State the blood parasite species.
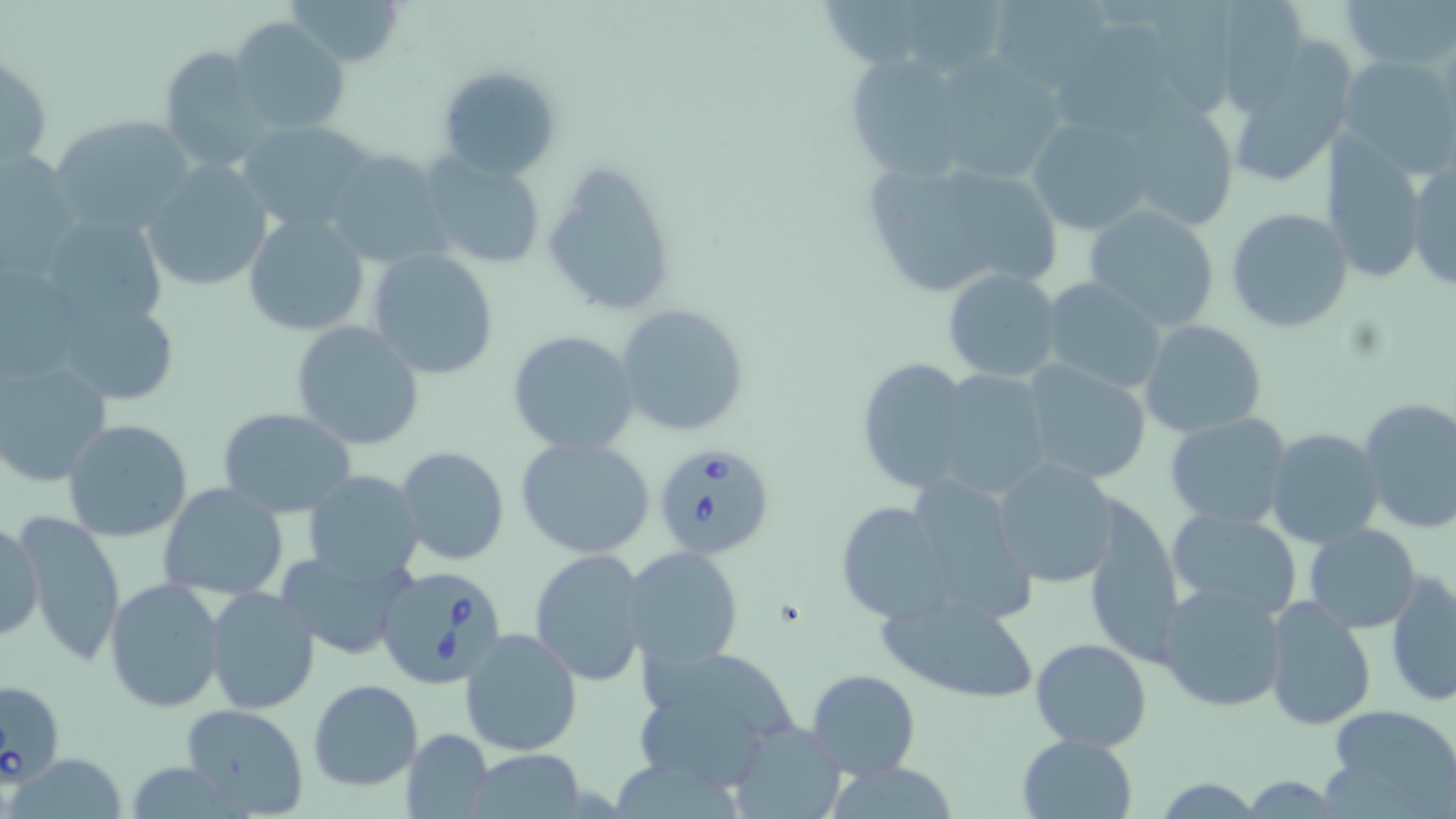
Babesia divergens.

preparation = thin blood film
image size = 1456×819 pixels
modality = light microscopy
magnification = 1000x
stain = May-Grünwald-Giemsa
Babesia divergens-infected red blood cell locations = approximate bounding boxes as [x1, y1, x2, y2] in pixels: [650, 440, 778, 561], [372, 562, 511, 692]
uninfected red blood cell locations = approximate bounding boxes as [x1, y1, x2, y2] in pixels: [286, 0, 408, 68], [902, 0, 1004, 81], [1225, 0, 1312, 117], [1342, 0, 1453, 74], [1150, 1, 1243, 114], [826, 2, 931, 69], [996, 2, 1112, 85], [228, 18, 351, 135], [1059, 19, 1176, 134], [1224, 44, 1357, 192], [157, 47, 277, 175], [1, 51, 52, 175], [842, 53, 981, 182], [1336, 53, 1456, 178], [949, 56, 1066, 182], [437, 65, 560, 179], [1108, 95, 1243, 235], [1024, 110, 1163, 238], [49, 113, 196, 231], [240, 119, 379, 234], [1317, 139, 1428, 282], [321, 148, 451, 270], [1, 149, 82, 270], [419, 154, 546, 268], [1407, 155, 1455, 293], [541, 158, 676, 317], [142, 160, 274, 292], [958, 167, 1063, 290], [870, 171, 986, 293], [1083, 202, 1221, 331], [1226, 207, 1354, 333], [34, 211, 170, 335], [242, 211, 371, 338], [366, 248, 500, 380], [943, 267, 1065, 383], [1038, 278, 1171, 393], [40, 288, 186, 411], [615, 302, 749, 437], [1139, 320, 1267, 438], [290, 321, 425, 450], [505, 330, 639, 456], [855, 355, 978, 492], [0, 357, 112, 487], [1018, 360, 1153, 486], [915, 367, 1060, 500], [1356, 396, 1456, 535], [216, 407, 357, 519], [1163, 411, 1293, 531], [62, 417, 194, 541], [193, 424, 333, 570], [1264, 428, 1385, 548], [514, 435, 657, 559], [395, 446, 509, 566], [989, 458, 1121, 588], [304, 471, 426, 588], [891, 471, 1040, 631], [157, 483, 290, 599], [1084, 496, 1186, 665], [831, 502, 949, 624], [1165, 507, 1305, 620], [13, 511, 128, 667], [1, 516, 42, 644], [1304, 524, 1422, 632], [529, 546, 653, 686], [621, 546, 745, 671], [278, 548, 416, 661], [1386, 571, 1455, 707], [104, 578, 227, 712], [1156, 581, 1290, 713], [204, 586, 320, 715], [876, 589, 1041, 704], [1263, 596, 1376, 732], [460, 628, 583, 756], [1028, 638, 1152, 752], [640, 649, 807, 740], [806, 668, 921, 779], [1, 678, 66, 785], [306, 679, 424, 791], [630, 700, 769, 783], [178, 703, 309, 818], [1324, 704, 1456, 813], [729, 719, 846, 818], [400, 728, 494, 819], [1016, 732, 1136, 817], [464, 749, 590, 817], [12, 751, 129, 819], [615, 758, 739, 819], [1154, 777, 1260, 817]
field of view = single